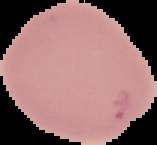
The area outside the segmented cell region is set to black. Image is 157×145 pixels. From a thin blood smear. Result: negative for Plasmodium parasites.